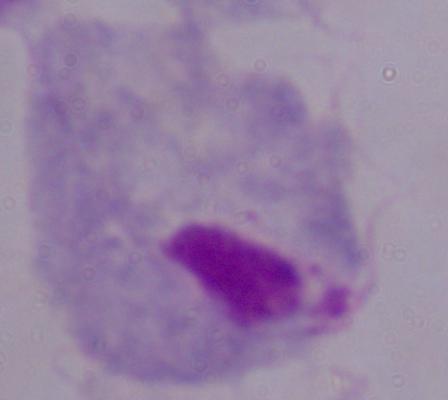
{
  "magnification": "1000x",
  "identification": "trichomonad",
  "modality": "photomicrograph"
}